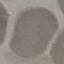
result: no malaria parasites seen
capture: smartphone through the microscope eyepiece
preparation: thin smear
image_type: automatically extracted cell patch, resized to 64 × 64 pixels
stain: Giemsa